Assess this cell for malaria.
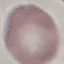

Uninfected.

capture: smartphone through the microscope eyepiece
image_type: automatically extracted cell patch, resized to 64 × 64 pixels
stain: Giemsa
preparation: thin smear